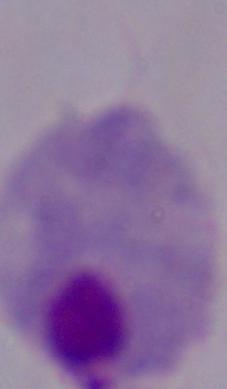

1000x magnification. A trichomonad is shown. Photomicrograph.